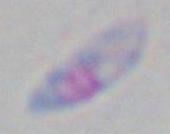
identification: Toxoplasma gondii
magnification: 1000x
modality: micrograph